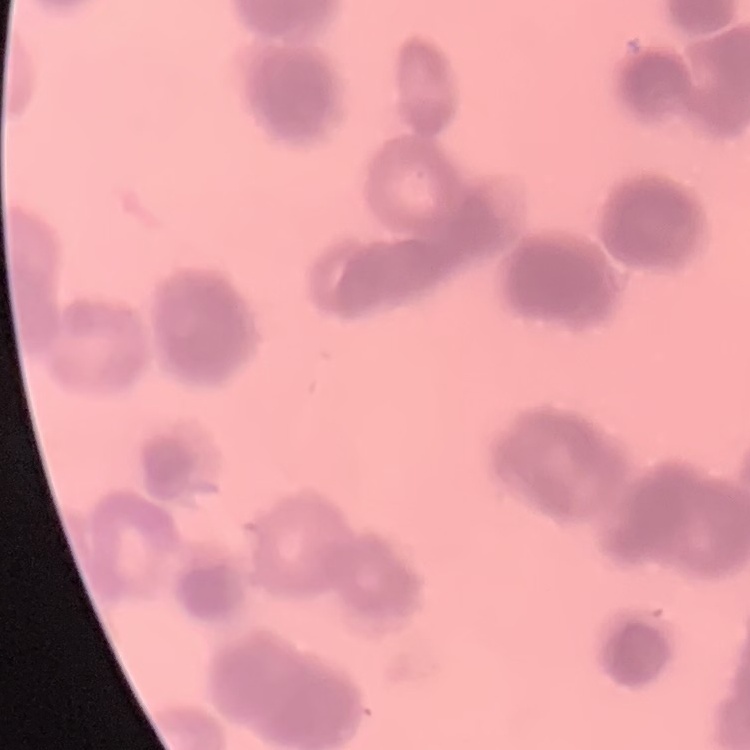

The red blood cells exhibit rouleaux formation. Square crop of a larger photomicrograph. Thin blood smear. Stained with either Field's or Giemsa.